Locate leukocytes (white blood cells).
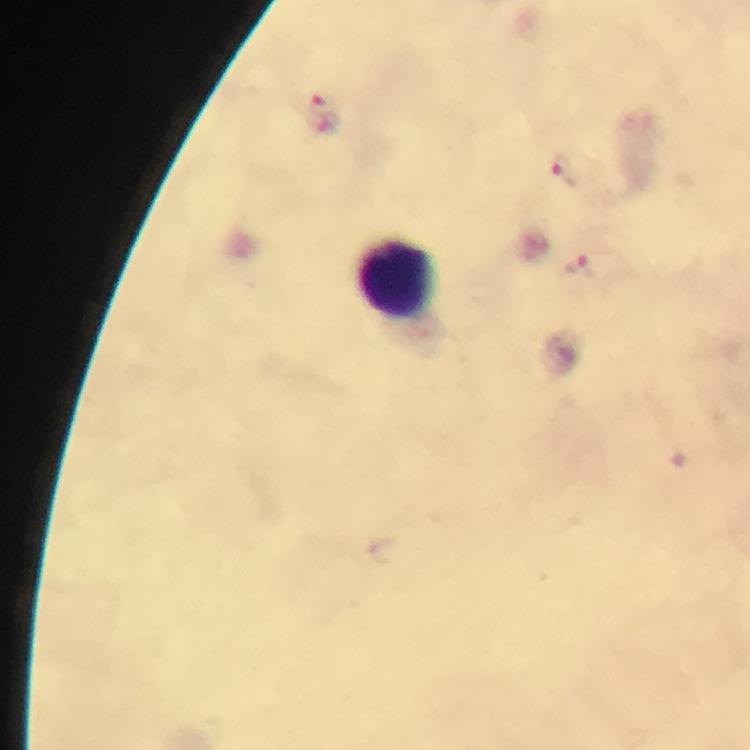

Approximate object centers, in pixels from the top-left corner.
Leukocytes: (x=398, y=281).

Plasmodium parasite locations = approximate object centers, in pixels from the top-left corner: (x=321, y=110), (x=566, y=176), (x=580, y=268)
stain = Giemsa
image size = 750×750 pixels
cropped from = a single field of view
capture = smartphone photograph through a microscope
preparation = thick smear
context = from a malaria diagnostic workup
magnification = 100x
immersion oil = used